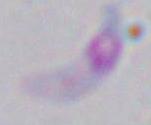
identification: Toxoplasma gondii
modality: micrograph
magnification: 1000x